Locate every blood parasite and identify its species.
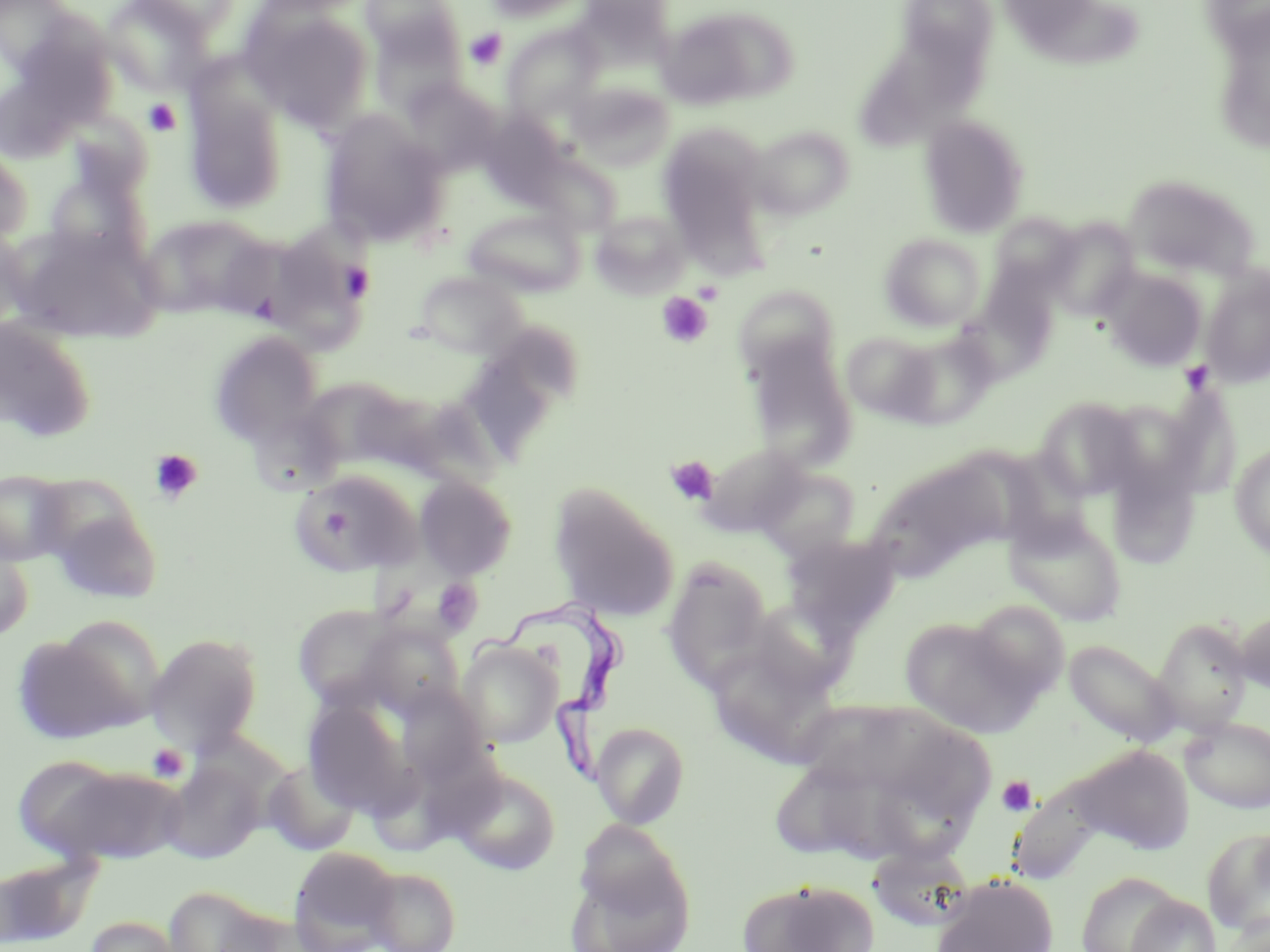

Approximate bounding boxes as (x1, y1, x2, y2) in pixels.
Trypanosoma brucei: (480, 599, 633, 792).
No Plasmodium falciparum, Plasmodium ovale, Plasmodium malariae, Plasmodium vivax, or Babesia divergens observed.

slide-level diagnosis = Trypanosoma brucei
modality = optical microscopy
platelet locations = approximate bounding boxes as (x1, y1, x2, y2) in pixels: (464, 28, 507, 70), (143, 98, 180, 136), (339, 261, 376, 302), (694, 281, 724, 304), (657, 292, 713, 348), (1179, 360, 1215, 394), (149, 449, 203, 505), (665, 456, 719, 506), (431, 578, 483, 636), (146, 743, 189, 782), (997, 775, 1037, 816)
stain = May-Grünwald-Giemsa
preparation = thin blood film
field of view = one of a larger specimen
magnification = 1000x
image size = 1270×952 pixels
uninfected red blood cell locations = approximate bounding boxes as (x1, y1, x2, y2) in pixels: (1, 0, 81, 78), (101, 0, 211, 95), (129, 0, 242, 36), (252, 0, 372, 16), (360, 0, 461, 62), (481, 0, 589, 23), (898, 1, 998, 73), (1024, 4, 1145, 77), (243, 6, 373, 130), (656, 8, 778, 110), (368, 16, 466, 115), (11, 20, 120, 127), (502, 25, 603, 123), (852, 41, 988, 152), (400, 79, 501, 173), (568, 82, 675, 171), (184, 89, 287, 215), (478, 112, 567, 203), (320, 113, 450, 248), (919, 114, 1029, 237), (750, 123, 856, 221), (657, 126, 767, 239), (0, 146, 32, 246), (531, 152, 622, 236), (44, 166, 150, 266), (1123, 173, 1261, 280), (463, 208, 585, 297), (592, 210, 690, 296), (137, 214, 271, 318), (989, 214, 1081, 296), (1043, 219, 1142, 323), (13, 227, 160, 343), (0, 228, 31, 332), (879, 233, 987, 331), (265, 250, 365, 355), (1200, 266, 1270, 389), (1102, 267, 1207, 371), (414, 270, 528, 359), (733, 283, 842, 383), (0, 317, 95, 442), (466, 325, 581, 456), (211, 330, 323, 443), (889, 330, 997, 428), (841, 331, 938, 422), (744, 339, 857, 470), (1144, 382, 1240, 501), (308, 385, 408, 464), (1034, 396, 1143, 501), (701, 442, 809, 537), (1230, 443, 1270, 558), (908, 464, 1011, 560), (1106, 465, 1200, 571), (755, 466, 861, 559), (292, 468, 422, 576), (0, 470, 72, 566), (413, 474, 518, 579), (549, 486, 678, 621), (48, 503, 162, 605), (1005, 510, 1127, 626), (781, 533, 901, 639), (0, 541, 33, 642), (662, 558, 773, 686), (965, 599, 1071, 705), (293, 603, 402, 710), (1234, 606, 1270, 695), (899, 615, 1040, 737), (1151, 617, 1252, 733), (360, 622, 464, 718), (146, 632, 264, 754), (11, 635, 141, 746), (1064, 639, 1179, 748), (457, 641, 562, 747), (712, 659, 844, 765), (396, 685, 491, 782), (302, 700, 416, 817), (801, 703, 913, 780), (1180, 717, 1270, 814), (591, 722, 690, 829), (895, 723, 994, 818), (1074, 745, 1197, 855), (13, 755, 128, 859), (262, 758, 360, 855), (160, 760, 264, 863), (46, 766, 183, 866), (450, 767, 560, 875), (873, 769, 976, 863), (776, 781, 845, 854), (1010, 782, 1108, 877), (1202, 825, 1270, 939), (288, 846, 400, 951), (873, 847, 978, 929), (0, 851, 103, 948), (564, 851, 696, 952), (365, 867, 461, 952), (1075, 871, 1186, 952), (931, 874, 1059, 952), (737, 878, 879, 952), (163, 885, 277, 952), (1126, 894, 1222, 952), (1224, 915, 1270, 952), (83, 916, 185, 952)